State which parasite is depicted.
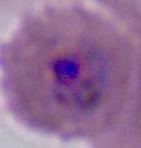
This is Plasmodium.

Summary:
  - Magnification: 400x or 1000x
  - Modality: photomicrograph